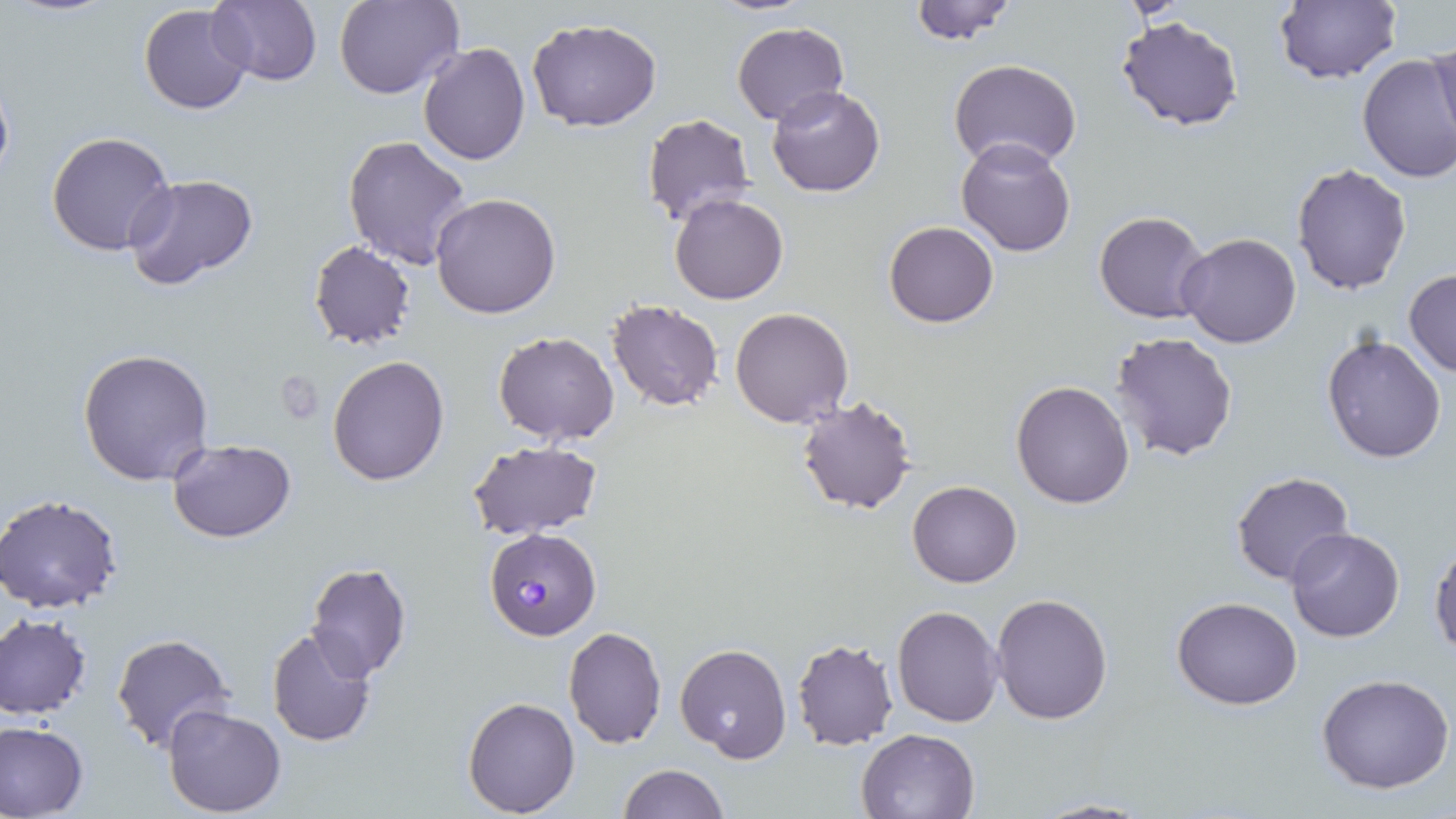
Summary:
  - Coordinate format: approximate bounding boxes as named x1/y1/x2/y2 corners in pixels
  - Uninfected red blood cell locations: (x1=208, y1=0, x2=322, y2=88), (x1=335, y1=0, x2=460, y2=100), (x1=906, y1=0, x2=1020, y2=45), (x1=1274, y1=0, x2=1401, y2=85), (x1=138, y1=3, x2=254, y2=115), (x1=1116, y1=15, x2=1246, y2=131), (x1=527, y1=20, x2=660, y2=133), (x1=731, y1=21, x2=848, y2=126), (x1=1429, y1=36, x2=1456, y2=155), (x1=418, y1=41, x2=531, y2=166), (x1=1357, y1=53, x2=1456, y2=185), (x1=948, y1=58, x2=1081, y2=171), (x1=766, y1=85, x2=887, y2=197), (x1=641, y1=111, x2=757, y2=231), (x1=46, y1=130, x2=178, y2=257), (x1=344, y1=134, x2=473, y2=271), (x1=955, y1=137, x2=1077, y2=257), (x1=1291, y1=163, x2=1412, y2=296), (x1=122, y1=174, x2=260, y2=290), (x1=431, y1=192, x2=562, y2=319), (x1=670, y1=193, x2=788, y2=305), (x1=1094, y1=211, x2=1212, y2=325), (x1=885, y1=221, x2=998, y2=328), (x1=1178, y1=234, x2=1302, y2=350), (x1=307, y1=241, x2=415, y2=349), (x1=1403, y1=269, x2=1456, y2=378), (x1=607, y1=299, x2=724, y2=412), (x1=731, y1=307, x2=852, y2=428), (x1=492, y1=331, x2=620, y2=443), (x1=1110, y1=332, x2=1239, y2=462), (x1=1320, y1=332, x2=1449, y2=465), (x1=78, y1=348, x2=216, y2=486), (x1=327, y1=355, x2=450, y2=486), (x1=1011, y1=381, x2=1134, y2=508), (x1=795, y1=394, x2=918, y2=516), (x1=167, y1=437, x2=295, y2=543), (x1=467, y1=441, x2=602, y2=539), (x1=1231, y1=470, x2=1357, y2=588), (x1=907, y1=479, x2=1022, y2=587), (x1=0, y1=495, x2=123, y2=613), (x1=1283, y1=529, x2=1404, y2=643), (x1=1429, y1=541, x2=1456, y2=660), (x1=305, y1=562, x2=413, y2=681), (x1=990, y1=593, x2=1113, y2=725), (x1=1172, y1=597, x2=1302, y2=710), (x1=891, y1=605, x2=1004, y2=726), (x1=0, y1=614, x2=93, y2=719), (x1=266, y1=625, x2=380, y2=749), (x1=561, y1=625, x2=666, y2=749), (x1=111, y1=633, x2=235, y2=753), (x1=790, y1=637, x2=900, y2=751), (x1=675, y1=643, x2=792, y2=764), (x1=1315, y1=674, x2=1455, y2=794), (x1=462, y1=696, x2=580, y2=816), (x1=162, y1=705, x2=287, y2=817), (x1=1, y1=721, x2=89, y2=819), (x1=856, y1=727, x2=982, y2=818), (x1=617, y1=764, x2=727, y2=819), (x1=1029, y1=798, x2=1152, y2=818)
  - Plasmodium falciparum-infected red blood cell locations: (x1=483, y1=528, x2=601, y2=641)
  - Slide-level diagnosis: Plasmodium falciparum
  - Preparation: thin blood film
  - Modality: light microscopy
  - Stain: May-Grünwald-Giemsa
  - Field of view: one of a larger specimen
  - Magnification: 1000x
  - Image size: 1456×819 pixels